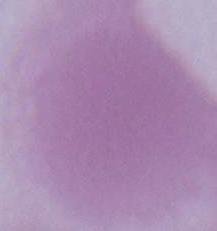 Photomicrograph. An erythrocyte is seen. Captured at 1000x magnification.